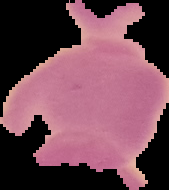
preparation = thin blood smear
image size = 169×190 pixels
image type = segmented cell region with the area outside set to black
result = no malaria parasites seen